Give the position of every malaria parasite and every leukocyte.
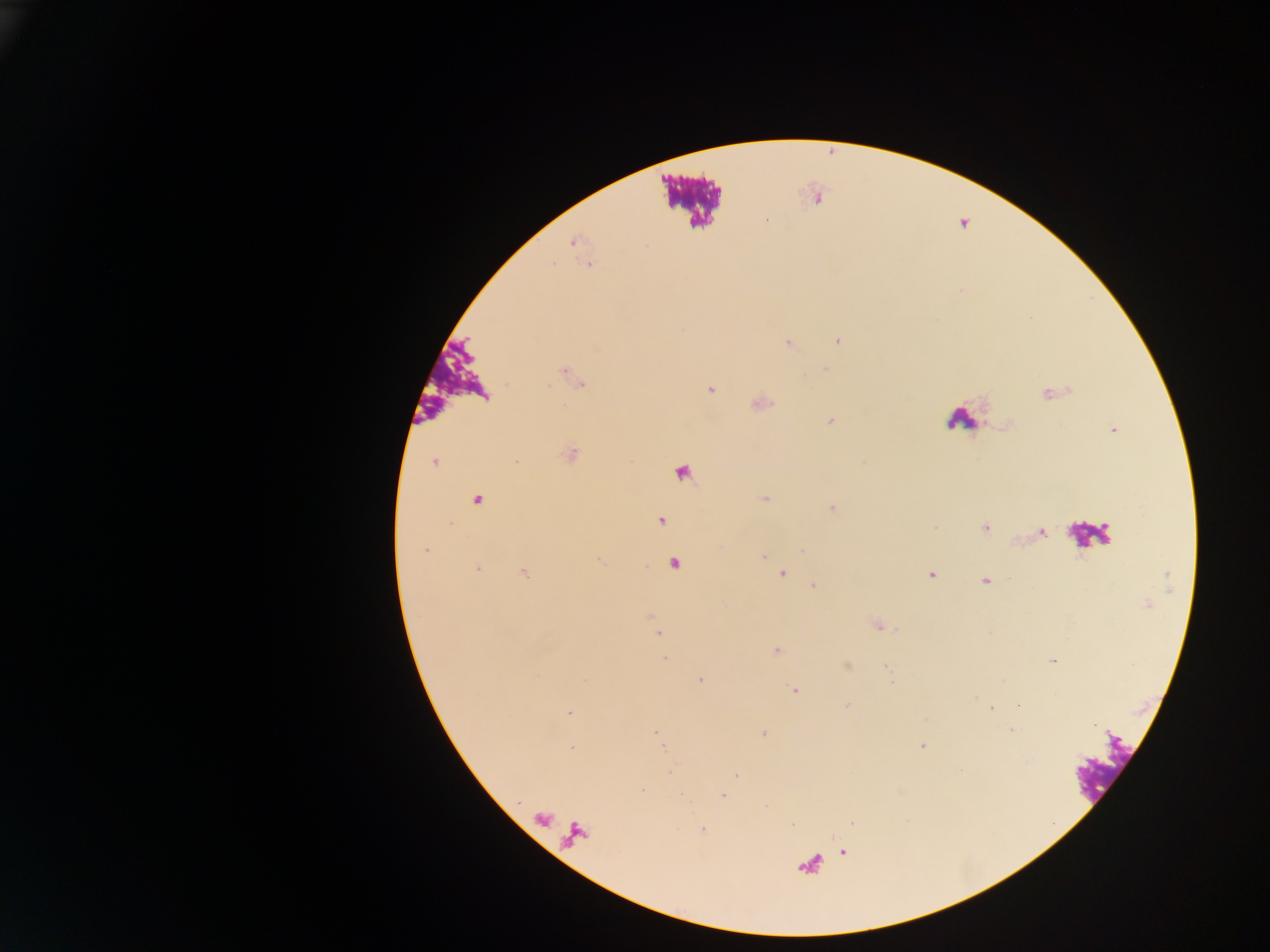
Approximate centers as [x, y] in pixels.
Malaria parasites: [573, 242], [589, 263], [837, 340], [788, 343], [825, 370], [569, 375], [578, 382], [710, 390], [1048, 393], [759, 403], [830, 420], [1114, 431], [568, 454], [434, 461], [680, 472], [764, 498], [476, 499], [831, 509], [660, 519], [984, 527], [1041, 533], [425, 550], [802, 550], [764, 556], [673, 562], [478, 567], [524, 572], [781, 573], [931, 574], [985, 580], [813, 585], [877, 624], [658, 632], [776, 651], [664, 658], [1052, 661], [845, 665], [886, 665], [700, 679], [794, 690], [1018, 704], [846, 705], [990, 709], [569, 711], [764, 732], [656, 734], [922, 746], [736, 775], [723, 795], [851, 822], [701, 830], [843, 852].
Leukocytes: [962, 419], [1091, 534].

Thick blood film. Photographed through a microscope with a mobile-phone camera. Single field of view. Image is 1270×952 pixels. Collected in Ghana.